Assess the morphology of the erythrocytes.
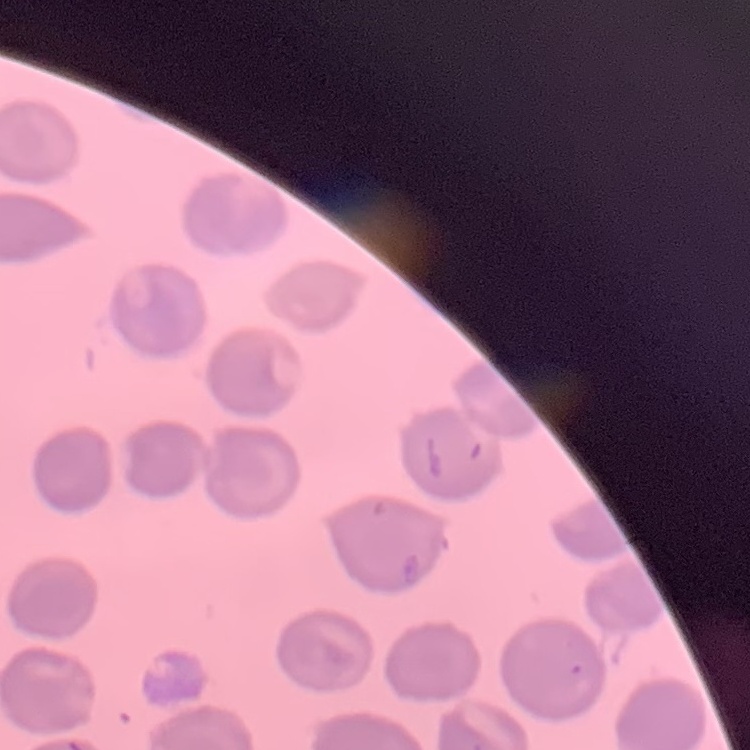

No rouleaux formation.

Summary:
  - Stain: Field's or Giemsa
  - Preparation: thin blood smear
  - Image type: one tile cut from a larger photomicrograph